State which parasite is depicted.
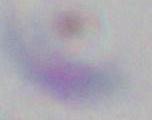

This is Toxoplasma gondii.

Summary:
  - Magnification: 1000x
  - Modality: photomicrograph